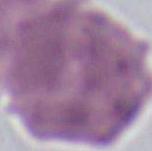

magnification = 1000x
modality = micrograph
identification = red blood cell